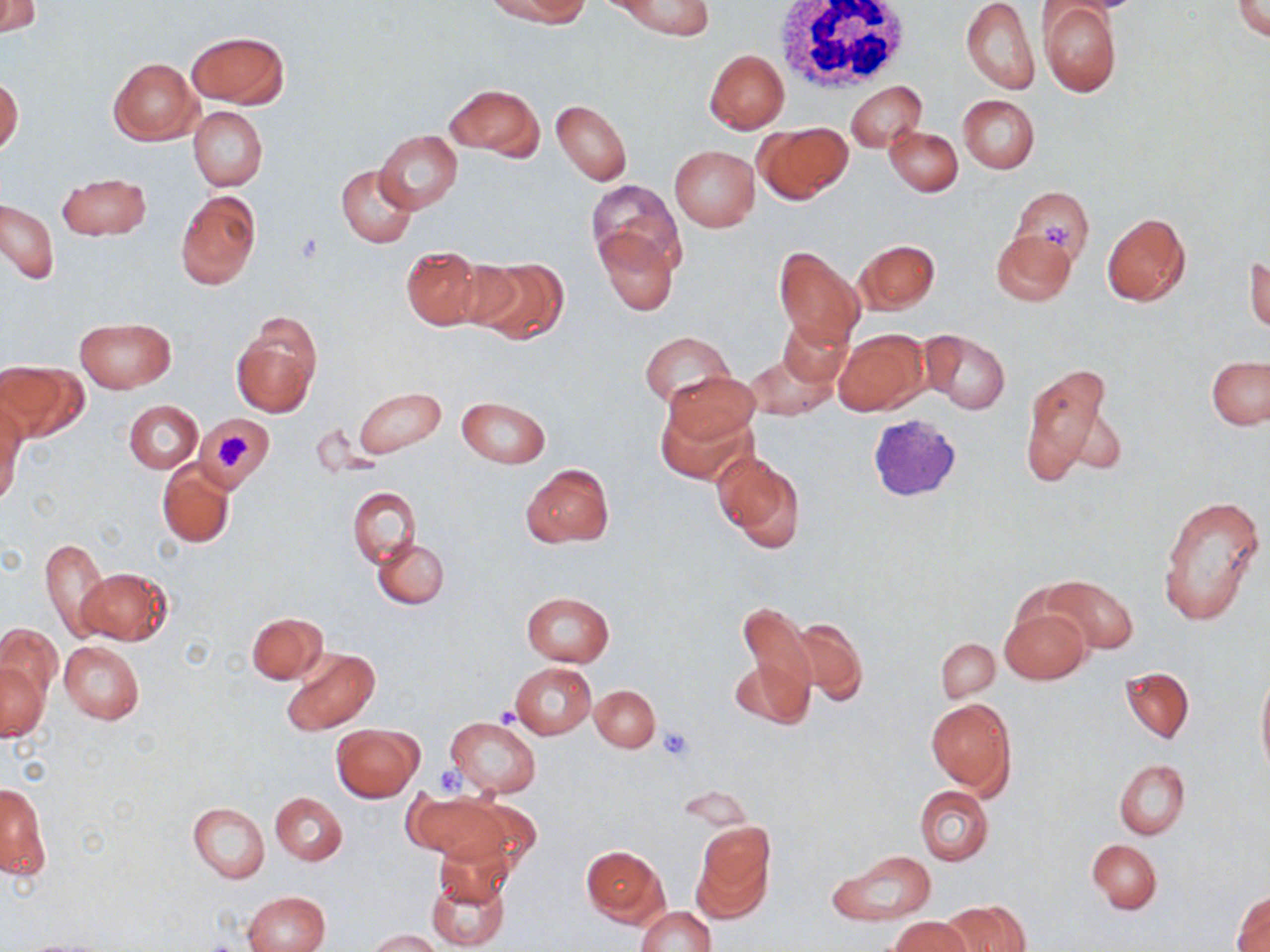

{
  "slide_level_diagnosis": "negative for blood parasites",
  "image_size": "1270×952 pixels",
  "magnification": "1000x",
  "stain": "May-Grünwald-Giemsa",
  "field_of_view": "one of a larger specimen",
  "modality": "light microscopy",
  "preparation": "thin blood film",
  "white_blood_cell_locations": "approximate bounding boxes as (x1,y1)-(x2,y2) corner pairs in pixels: (771,0)-(913,95)",
  "uninfected_red_blood_cell_locations": "approximate bounding boxes as (x1,y1)-(x2,y2) corner pairs in pixels: (0,0)-(40,36), (609,0)-(714,38), (960,0)-(1039,94), (1231,0)-(1270,42), (494,2)-(590,27), (1038,3)-(1122,98), (187,30)-(288,109), (704,50)-(790,134), (108,58)-(201,144), (0,77)-(23,156), (845,81)-(926,152), (444,84)-(544,159), (957,94)-(1039,174), (551,100)-(631,186), (189,107)-(267,191), (754,122)-(851,205), (885,125)-(963,197), (375,130)-(462,214), (669,145)-(760,231), (336,165)-(417,248), (56,172)-(151,241), (588,180)-(682,273), (1009,185)-(1094,264), (176,190)-(261,291), (1,200)-(59,284), (1102,211)-(1191,307), (595,228)-(679,316), (991,229)-(1076,306), (854,240)-(939,314), (772,245)-(866,350), (400,248)-(483,329), (1245,251)-(1269,334), (471,256)-(569,343), (230,313)-(320,419), (75,317)-(174,392), (777,317)-(852,388), (833,328)-(929,416), (919,329)-(1011,415), (640,332)-(734,408), (745,348)-(837,421), (1206,356)-(1270,430), (2,357)-(87,439), (1019,362)-(1119,488), (665,372)-(759,447), (351,386)-(446,460), (456,395)-(551,469), (124,400)-(202,474), (0,401)-(24,504), (655,401)-(756,487), (197,415)-(271,488), (713,450)-(806,553), (156,461)-(234,549), (520,464)-(614,548), (349,486)-(420,568), (1159,495)-(1266,627), (373,537)-(449,609), (41,538)-(110,641), (78,567)-(172,645), (1044,575)-(1138,654), (520,592)-(614,667), (735,601)-(817,721), (1000,606)-(1090,685), (246,612)-(327,683), (790,618)-(868,706), (0,625)-(61,702), (937,638)-(1000,701), (59,641)-(144,725), (281,648)-(379,736), (729,660)-(812,728), (2,662)-(48,741), (510,663)-(596,738), (1120,666)-(1194,743), (1256,667)-(1269,779), (591,683)-(660,751), (926,697)-(1016,795), (445,716)-(543,799), (331,724)-(424,802), (1115,759)-(1190,840), (1,784)-(49,883), (916,786)-(993,865), (271,792)-(347,865), (407,792)-(509,865), (444,796)-(542,871), (188,802)-(270,883), (693,823)-(774,919), (433,840)-(515,909), (1087,840)-(1162,913), (581,846)-(669,926), (829,852)-(936,925), (425,868)-(513,950), (1233,890)-(1270,951), (242,891)-(329,952), (942,899)-(1031,952), (636,906)-(715,952), (889,916)-(970,952), (368,929)-(440,952)",
  "platelet_locations": "approximate bounding boxes as (x1,y1)-(x2,y2) corner pairs in pixels: (1044,217)-(1068,249), (215,433)-(256,473), (657,725)-(694,761), (434,765)-(465,796)"
}